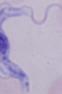
Summary:
  - Identification: trypanosome
  - Magnification: 1000x
  - Modality: photomicrograph